Assess this cell for malaria.
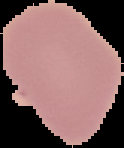

Uninfected.

image type = cell region segmented out of the field of view; surrounding area masked to black
image size = 124×148 pixels
preparation = thin blood smear